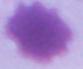
magnification = 1000x
modality = micrograph
identification = red blood cell